Name the parasite shown.
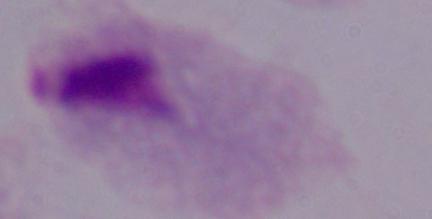
This is a trichomonad.

Micrograph. 1000x magnification.